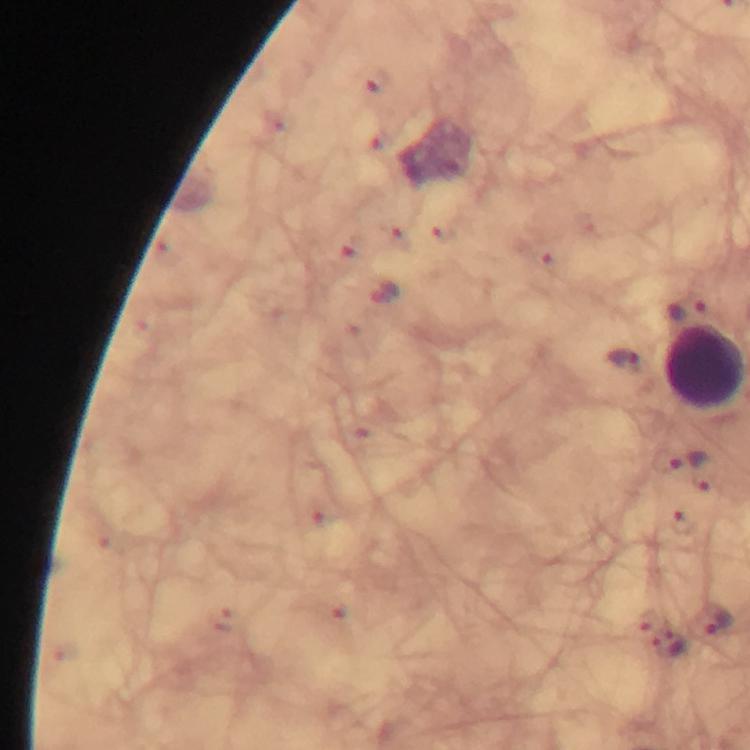 Approximate centers as {x, y} in pixels. Leukocyte locations: {706, 365}. Malaria parasite locations: {379, 83}, {386, 141}, {396, 235}, {444, 235}, {349, 257}, {547, 262}, {383, 296}, {626, 361}, {662, 459}, {703, 472}, {681, 524}, {226, 621}, {712, 622}. Immersion oil was used. Image is 750×750 pixels. Giemsa stain. Thick blood film. Cropped region of a single field of view. Photographed with a smartphone mounted on the microscope. From a diagnostic examination for malaria. 100x magnification.